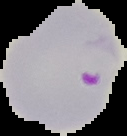
{
  "preparation": "thin blood film",
  "malaria_status": "parasitized",
  "image_type": "segmented cell region with the area outside set to black",
  "image_size": "127×136 pixels"
}